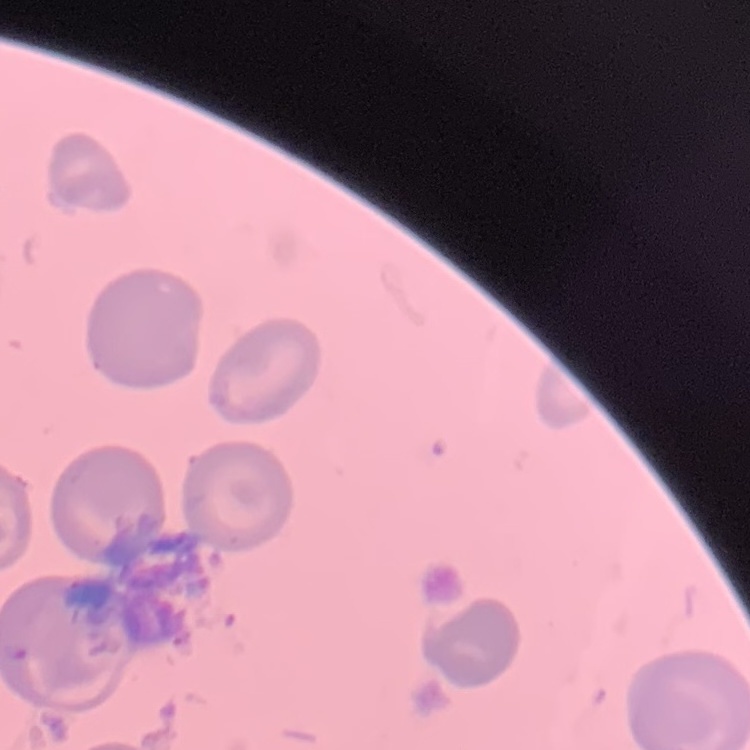

erythrocyte morphology = no rouleaux formation
preparation = thin blood smear
image type = one tile cut from a larger photomicrograph
stain = Field's or Giemsa